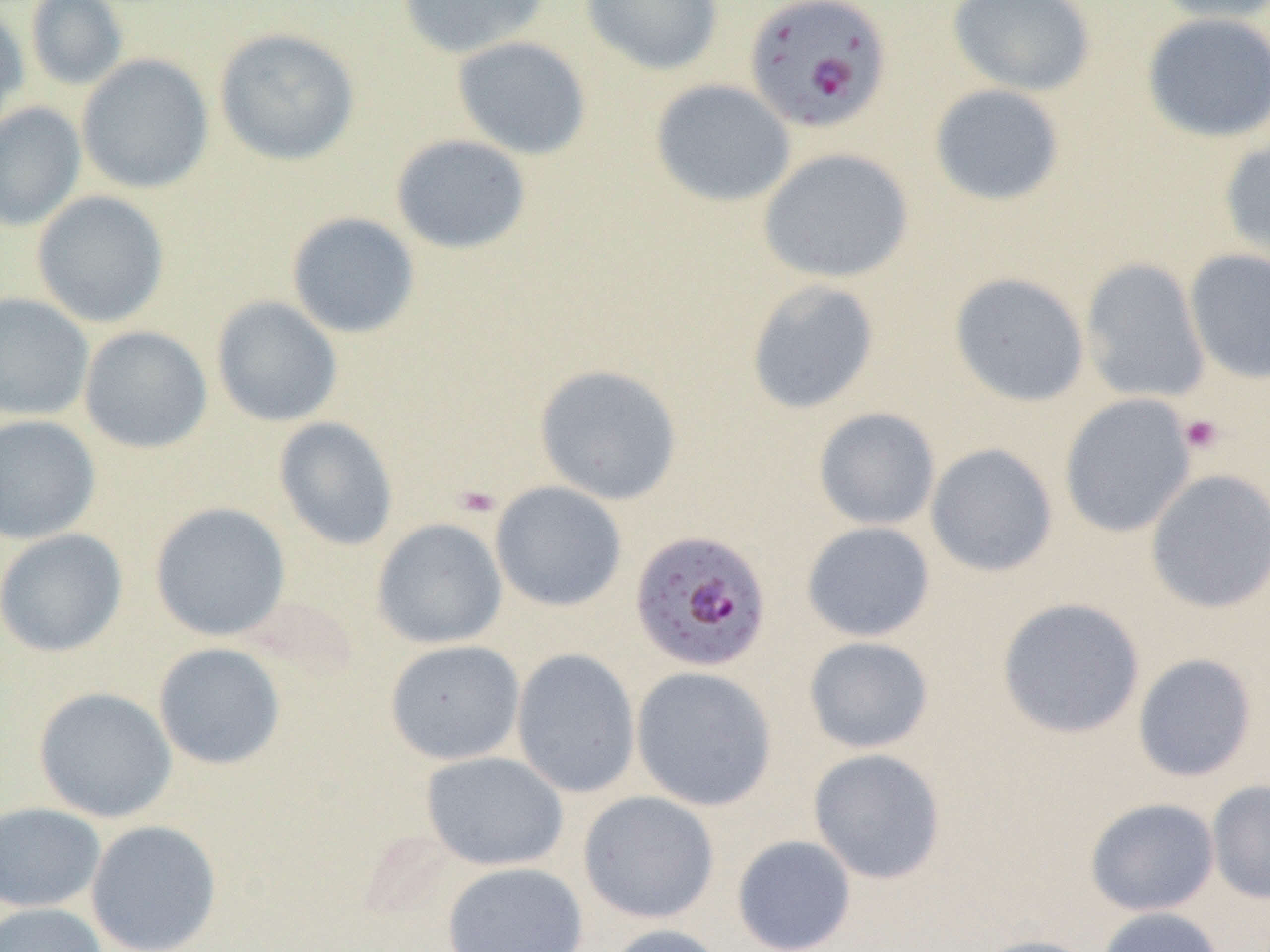

Approximate bounding boxes as (x1, y1, x2, y2) in pixels. Uninfected red blood cell locations: (25, 0, 128, 91), (397, 0, 551, 59), (580, 0, 724, 76), (947, 0, 1096, 97), (1147, 0, 1270, 24), (0, 5, 29, 135), (1141, 12, 1270, 143), (214, 27, 360, 166), (452, 36, 592, 160), (76, 53, 214, 194), (650, 79, 796, 208), (928, 83, 1066, 207), (0, 101, 86, 232), (391, 134, 532, 255), (1218, 136, 1270, 267), (758, 147, 914, 284), (31, 190, 170, 328), (285, 211, 421, 339), (1184, 249, 1270, 384), (1080, 257, 1210, 403), (949, 272, 1090, 407), (745, 278, 881, 415), (0, 293, 94, 421), (211, 296, 343, 427), (79, 325, 213, 454), (534, 363, 683, 505), (1059, 393, 1196, 538), (812, 407, 941, 530), (0, 414, 101, 544), (273, 417, 399, 551), (925, 442, 1058, 578), (1144, 468, 1270, 614), (490, 481, 628, 612), (149, 502, 291, 641), (372, 517, 508, 649), (801, 521, 935, 642), (0, 527, 128, 657), (996, 597, 1145, 739), (802, 636, 934, 754), (384, 639, 525, 765), (153, 642, 286, 770), (510, 648, 642, 799), (1132, 653, 1258, 783), (631, 666, 778, 811), (33, 686, 178, 823), (808, 748, 946, 884), (420, 750, 569, 871), (1207, 780, 1270, 904), (577, 791, 720, 924), (1085, 797, 1220, 916), (0, 801, 106, 913), (85, 819, 223, 952), (731, 834, 857, 951), (442, 861, 588, 952), (0, 903, 108, 952), (1095, 907, 1226, 952), (600, 923, 728, 952), (969, 934, 1102, 952). Platelet locations: (1179, 414, 1224, 455), (454, 484, 503, 519). Plasmodium falciparum-infected red blood cell locations: (743, 0, 893, 134), (630, 526, 773, 670). Slide-level diagnosis: Plasmodium falciparum. Light microscopy. One field of a larger specimen. Image is 1270×952 pixels. Captured at 1000x magnification. Thin blood smear.